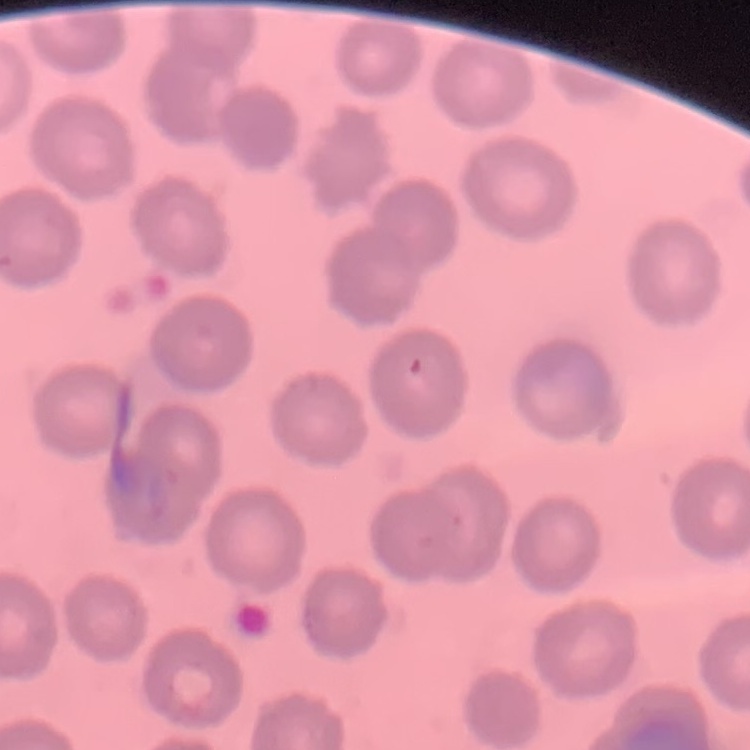
erythrocyte_morphology: no rouleaux formation
image_type: one tile cut from a larger photomicrograph
stain: Field's or Giemsa
preparation: thin blood smear